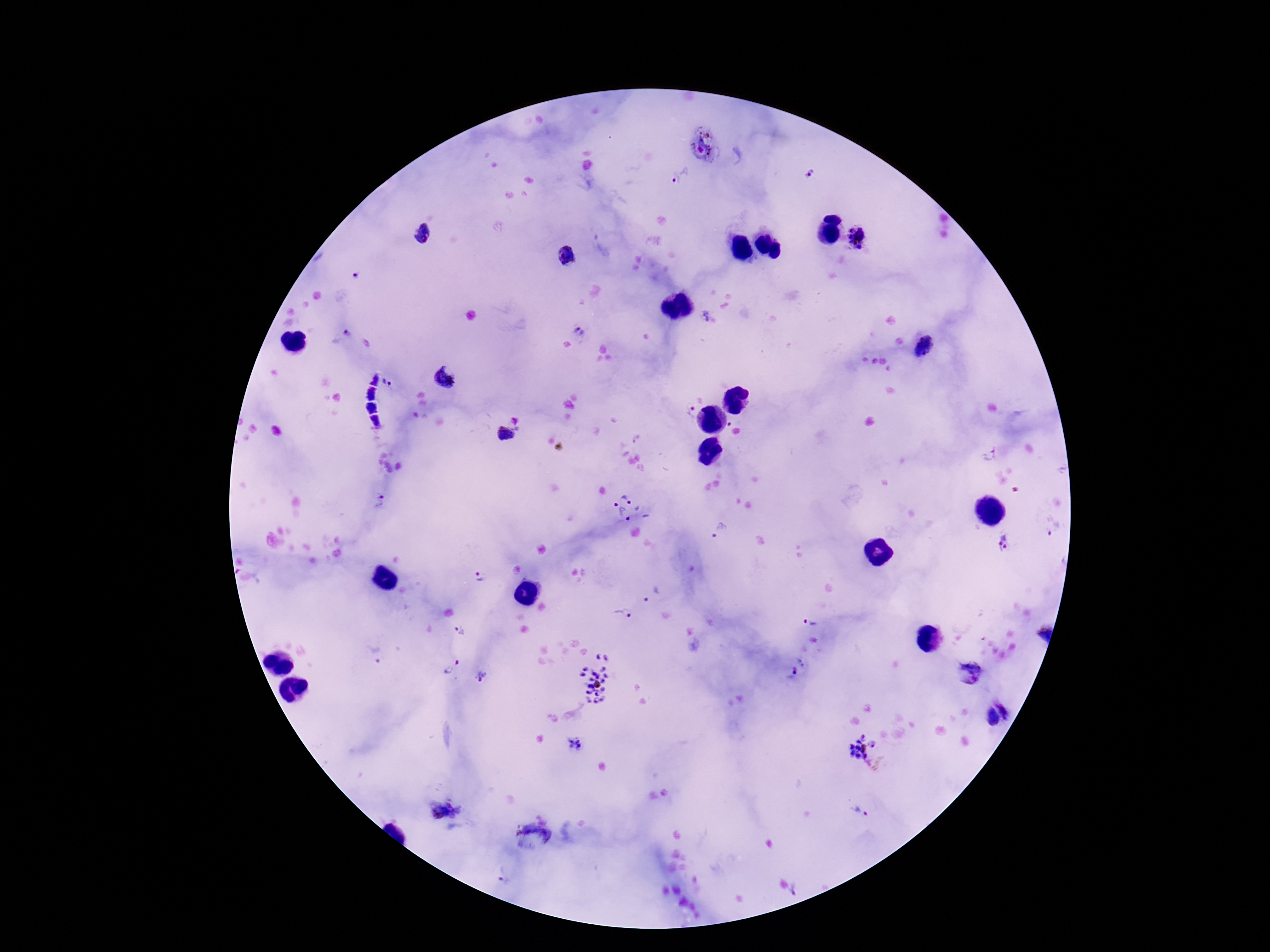

{
  "preparation": "thick peripheral-blood smear",
  "capture": "smartphone camera through the microscope eyepiece",
  "plasmodium_parasite_locations": "approximate object centers, in pixels from the top-left corner: (x=703, y=147), (x=808, y=173), (x=680, y=174), (x=421, y=235), (x=857, y=239), (x=567, y=255), (x=356, y=275), (x=707, y=318), (x=578, y=331), (x=340, y=338), (x=925, y=347), (x=444, y=380), (x=387, y=382), (x=690, y=412), (x=505, y=433), (x=988, y=456), (x=381, y=502), (x=626, y=508), (x=719, y=531), (x=1055, y=531), (x=1006, y=542), (x=478, y=575), (x=652, y=594), (x=622, y=614), (x=811, y=619), (x=461, y=631), (x=1044, y=634), (x=375, y=654), (x=450, y=666), (x=796, y=668), (x=971, y=672), (x=482, y=677), (x=595, y=679), (x=996, y=717), (x=575, y=744), (x=863, y=751), (x=443, y=812), (x=859, y=812), (x=530, y=841), (x=503, y=877), (x=795, y=890)",
  "stain": "Giemsa",
  "patient_malaria_status": "positive",
  "image_size": "1270×952 pixels",
  "field_of_view": "single",
  "magnification": "100x"
}